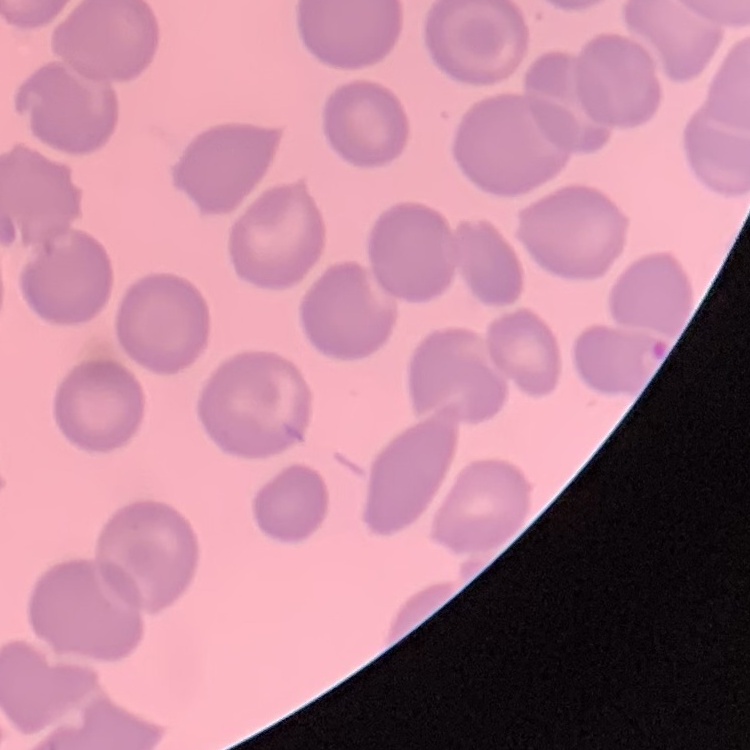
Summary:
  - Red blood cell morphology: no rouleaux formation
  - Preparation: thin blood smear
  - Image type: square crop of a larger photomicrograph
  - Stain: Field's or Giemsa